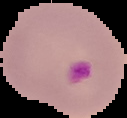
Segmented cell region on a black background. Malaria status: parasitized. From a thin blood film. Image is 127×118 pixels.